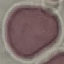
Summary:
  - Malaria status: uninfected
  - Preparation: thin smear
  - Capture: smartphone through the microscope eyepiece
  - Image type: automatically extracted cell patch, resized to 64 × 64 pixels
  - Stain: Giemsa